State the preparation type.
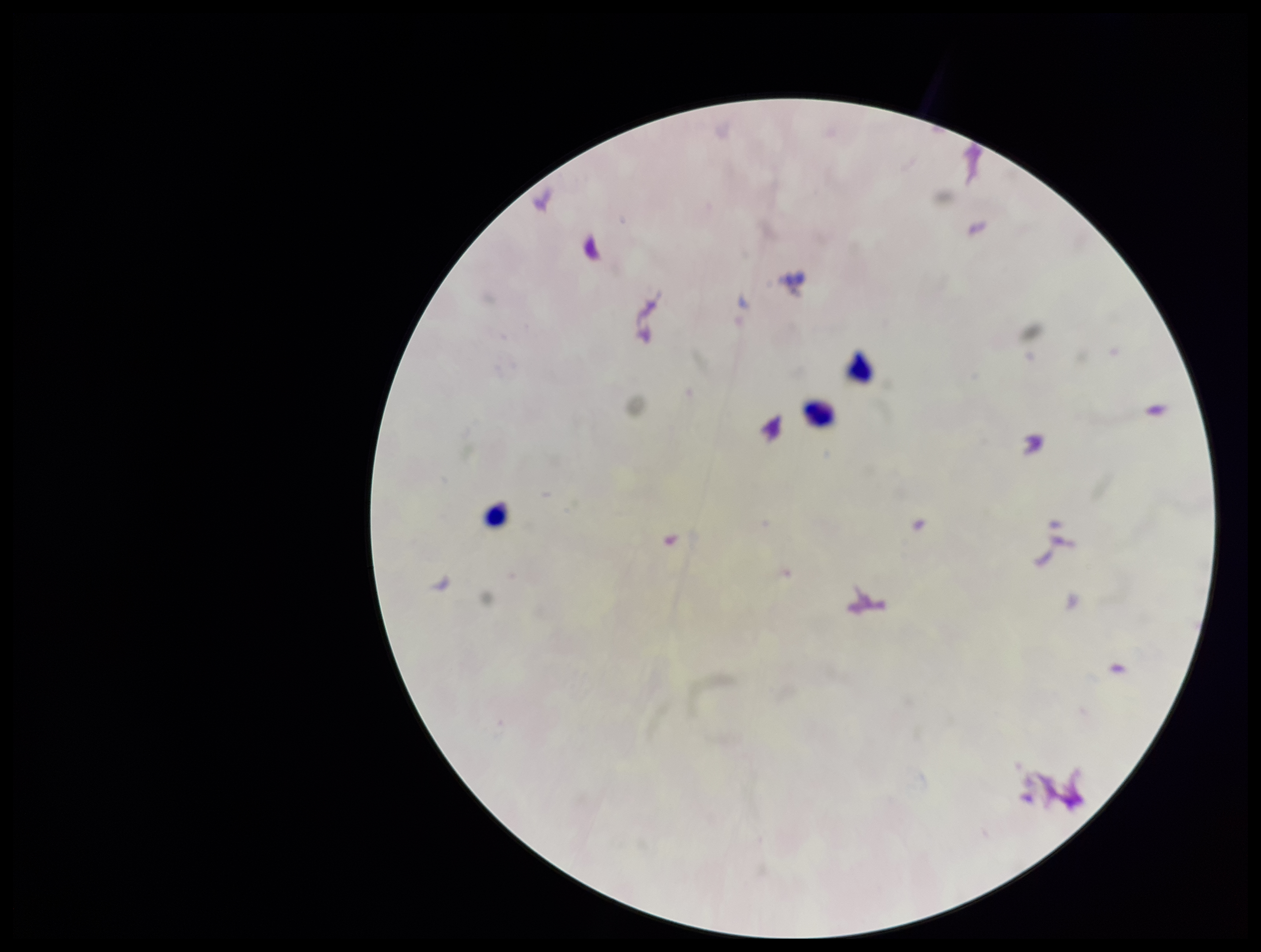

Thick.

stain = Giemsa
Plasmodium parasites = none detected
capture = smartphone photograph through the microscope eyepiece
field of view = one from this slide
parasite count = 0
image size = 1261×952 pixels
patient malaria status = negative
leukocyte count = 3